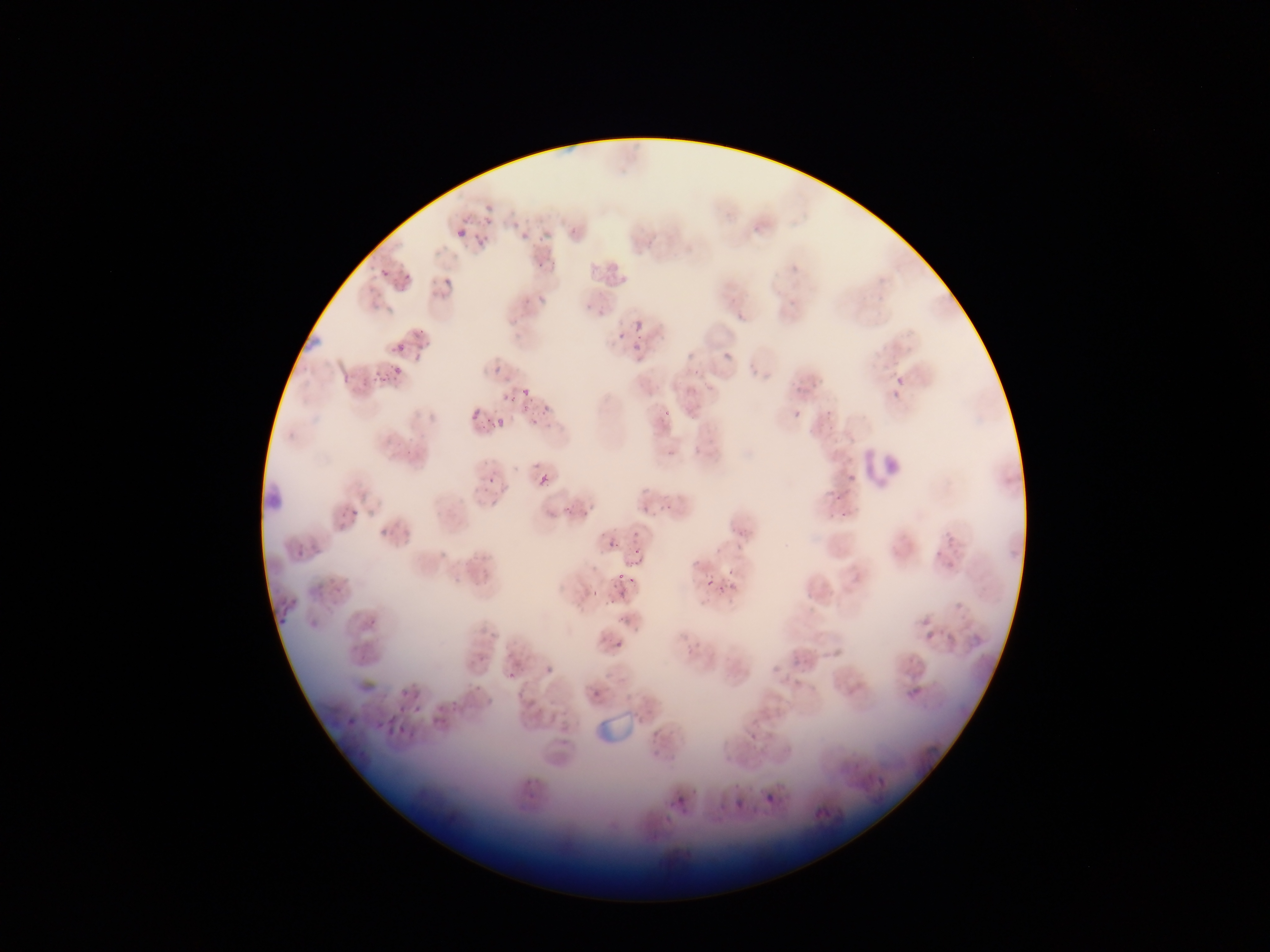

malaria_parasite_locations: 'approximate bounding boxes as left top right bottom in pixels: 484 204 493 214; 457 228 467 239; 523 231 532 240; 478 236 488 246; 539 260 549 269; 380 268 390 279; 402 274 411 285; 444 278 452 288; 634 320 643 330; 299 330 322 351; 618 333 627 341; 635 342 643 351; 393 343 407 356; 724 353 732 361; 393 365 401 375; 491 366 501 375; 370 367 390 385; 893 380 908 389; 521 389 529 399; 885 392 904 403; 502 393 512 402; 541 403 551 413; 793 409 802 419; 470 410 479 420; 657 414 675 428; 495 417 505 428; 667 449 676 458; 848 474 855 483; 484 475 495 485; 539 475 548 485; 561 503 578 520; 641 504 650 515; 341 505 359 522; 380 529 389 537; 606 536 623 550; 289 543 306 564; 633 550 643 561; 612 569 625 586; 324 570 345 597; 627 575 637 586; 705 575 715 585; 722 578 742 595; 705 579 714 588; 591 587 601 600; 278 600 298 626; 924 630 935 642; 971 635 983 647; 614 641 623 650; 507 671 515 681; 591 689 603 702; 400 695 417 722; 428 705 456 727; 381 714 399 737; 750 732 759 740; 874 773 889 790; 672 789 688 807; 764 790 779 806; 730 797 744 808; 811 801 833 822'
field_of_view: single
capture: mobile-phone photograph through a microscope
country: Ghana
preparation: thin blood film
image_size: 1270×952 pixels
leukocyte_locations: 'approximate bounding boxes as left top right bottom in pixels: 861 439 909 490'